Locate every malaria parasite.
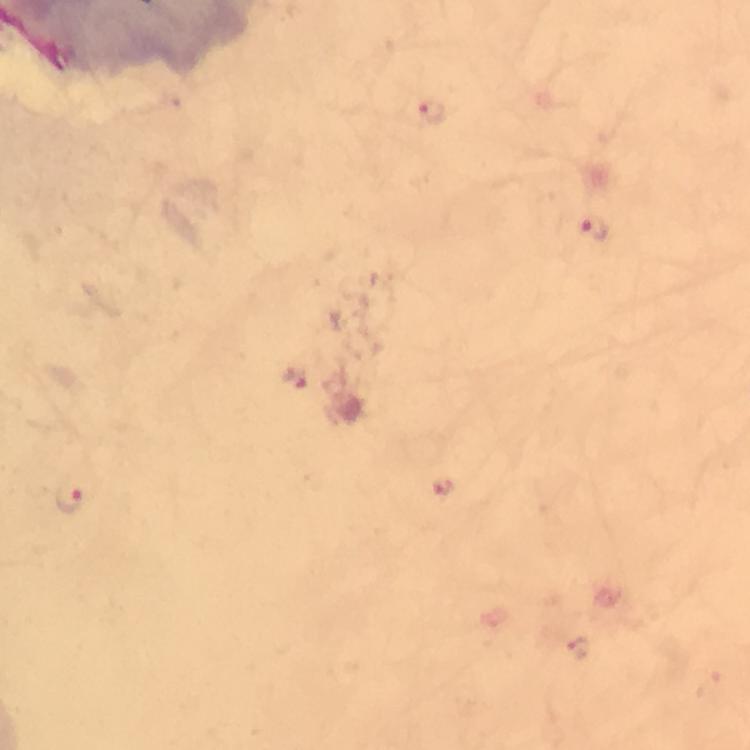

Approximate centers as [x, y] in pixels.
Malaria parasites: [432, 111], [591, 230], [295, 379], [445, 488], [69, 496], [579, 649].

Immersion oil applied. From a diagnostic examination for malaria. At 100x magnification. A crop from one field of view. Giemsa stain. Photographed with a smartphone mounted on the microscope. Image is 750×750 pixels. Thick blood film.